Give the extent of all uninfected red blood cells.
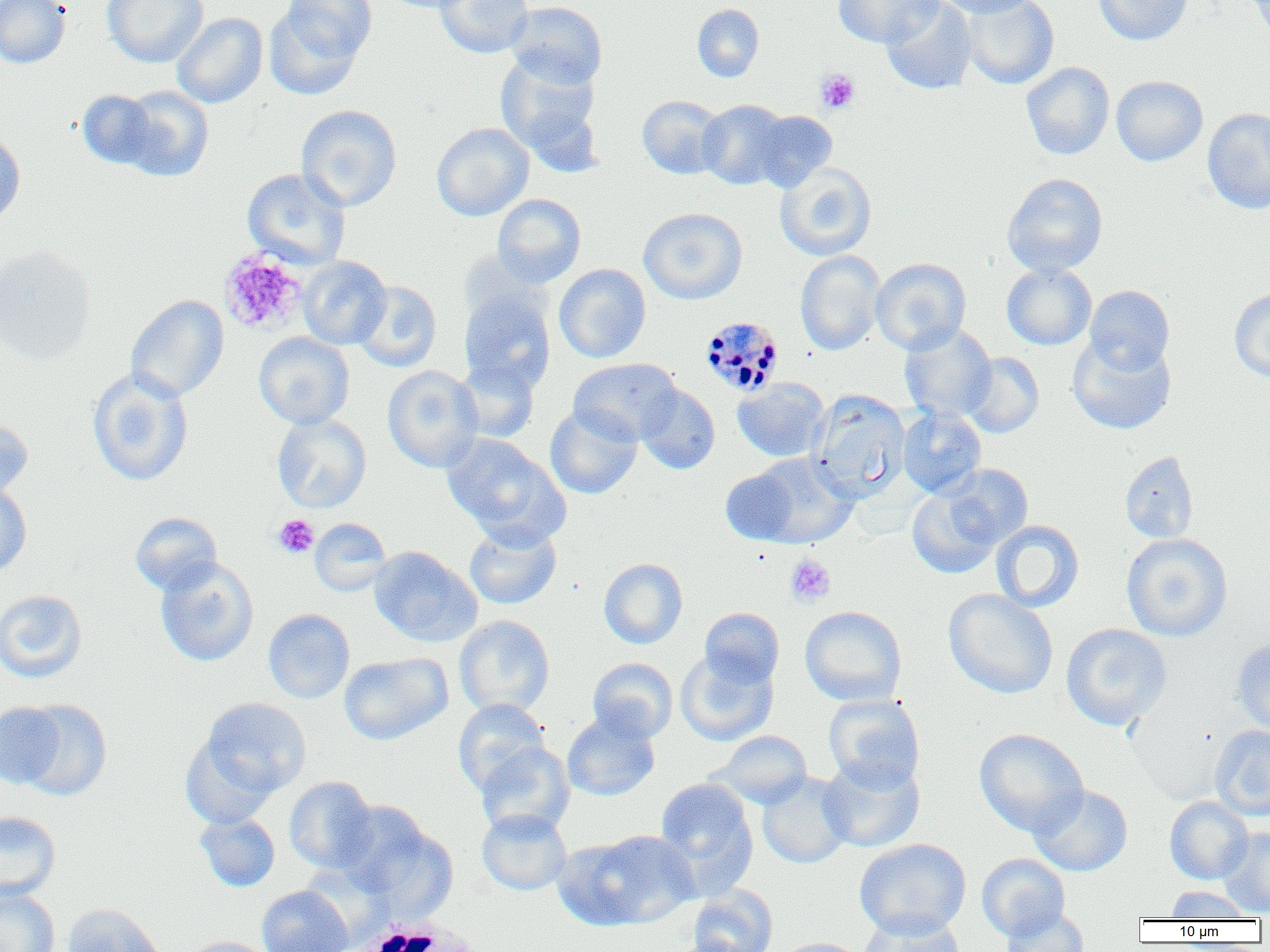

Approximate bounding boxes as [x1, y1, x2, y2] in pixels.
Uninfected red blood cells: [0, 0, 71, 68], [102, 0, 208, 67], [381, 0, 477, 13], [434, 0, 533, 58], [833, 0, 944, 48], [881, 0, 977, 94], [933, 0, 1040, 17], [960, 0, 1059, 89], [1093, 0, 1194, 46], [1248, 0, 1270, 42], [505, 1, 607, 89], [692, 3, 764, 83], [263, 4, 367, 100], [172, 12, 268, 108], [494, 53, 602, 160], [1021, 62, 1114, 160], [1111, 75, 1208, 166], [117, 85, 214, 182], [77, 90, 159, 170], [637, 95, 727, 179], [698, 99, 790, 189], [296, 105, 402, 211], [1202, 107, 1270, 214], [751, 110, 838, 192], [431, 122, 533, 221], [0, 130, 26, 228], [774, 163, 877, 261], [242, 168, 351, 269], [1002, 172, 1108, 276], [492, 194, 586, 287], [638, 208, 747, 305], [0, 247, 95, 364], [795, 250, 885, 356], [298, 256, 391, 349], [871, 258, 971, 355], [554, 263, 651, 363], [1001, 263, 1097, 350], [352, 280, 442, 372], [1084, 285, 1174, 374], [1229, 286, 1270, 383], [459, 289, 555, 392], [126, 295, 229, 402], [898, 324, 997, 422], [253, 332, 354, 429], [1067, 334, 1176, 435], [961, 353, 1044, 438], [453, 358, 540, 443], [568, 358, 683, 445], [383, 366, 483, 472], [87, 368, 193, 487], [733, 378, 830, 462], [635, 384, 720, 474], [808, 390, 910, 501], [545, 405, 643, 500], [897, 407, 987, 498], [272, 414, 372, 513], [0, 418, 33, 500], [442, 433, 567, 544], [1120, 450, 1199, 544], [743, 452, 859, 549], [942, 464, 1033, 549], [720, 467, 802, 544], [0, 482, 32, 577], [906, 487, 1001, 579], [129, 512, 222, 596], [309, 518, 392, 596], [990, 520, 1084, 612], [464, 523, 562, 609], [1121, 533, 1232, 642], [370, 547, 482, 646], [155, 557, 258, 667], [598, 558, 688, 649], [943, 588, 1058, 699], [0, 590, 87, 682], [799, 606, 907, 706], [699, 607, 785, 688], [263, 608, 355, 704], [453, 615, 555, 717], [1060, 623, 1172, 731], [1232, 639, 1270, 737], [676, 649, 778, 746], [339, 653, 452, 745], [588, 658, 678, 743], [823, 694, 925, 791], [200, 697, 311, 799], [453, 698, 551, 797], [13, 699, 112, 801], [0, 702, 67, 790], [562, 712, 660, 801], [1210, 725, 1270, 821], [974, 728, 1089, 837], [709, 730, 813, 809], [180, 739, 277, 829], [475, 741, 575, 837], [818, 756, 925, 853], [756, 771, 854, 869], [284, 776, 379, 873], [654, 777, 758, 897], [1029, 784, 1133, 877], [1164, 796, 1253, 884], [338, 807, 457, 915], [477, 808, 572, 895], [0, 810, 61, 902], [194, 812, 280, 892], [1217, 828, 1270, 916], [559, 829, 699, 931], [854, 838, 971, 938], [976, 853, 1071, 940], [257, 884, 353, 952], [687, 885, 777, 952], [1167, 886, 1254, 920], [0, 889, 60, 952], [62, 904, 166, 952], [1000, 906, 1090, 952], [857, 913, 966, 951], [182, 937, 277, 952], [774, 937, 869, 952].

Platelet locations: [815, 68, 860, 114], [219, 249, 307, 335], [272, 514, 319, 559], [785, 554, 836, 607]. White blood cell locations: [342, 915, 492, 951]. Plasmodium malariae-infected red blood cell locations: [700, 316, 786, 396]. Slide-level diagnosis: Plasmodium malariae. Image is 1270×952 pixels. 1000x magnification. One field of a larger specimen. Thin blood film. Optical microscopy.